Give the extent of all Plasmodium falciparum-infected red blood cells.
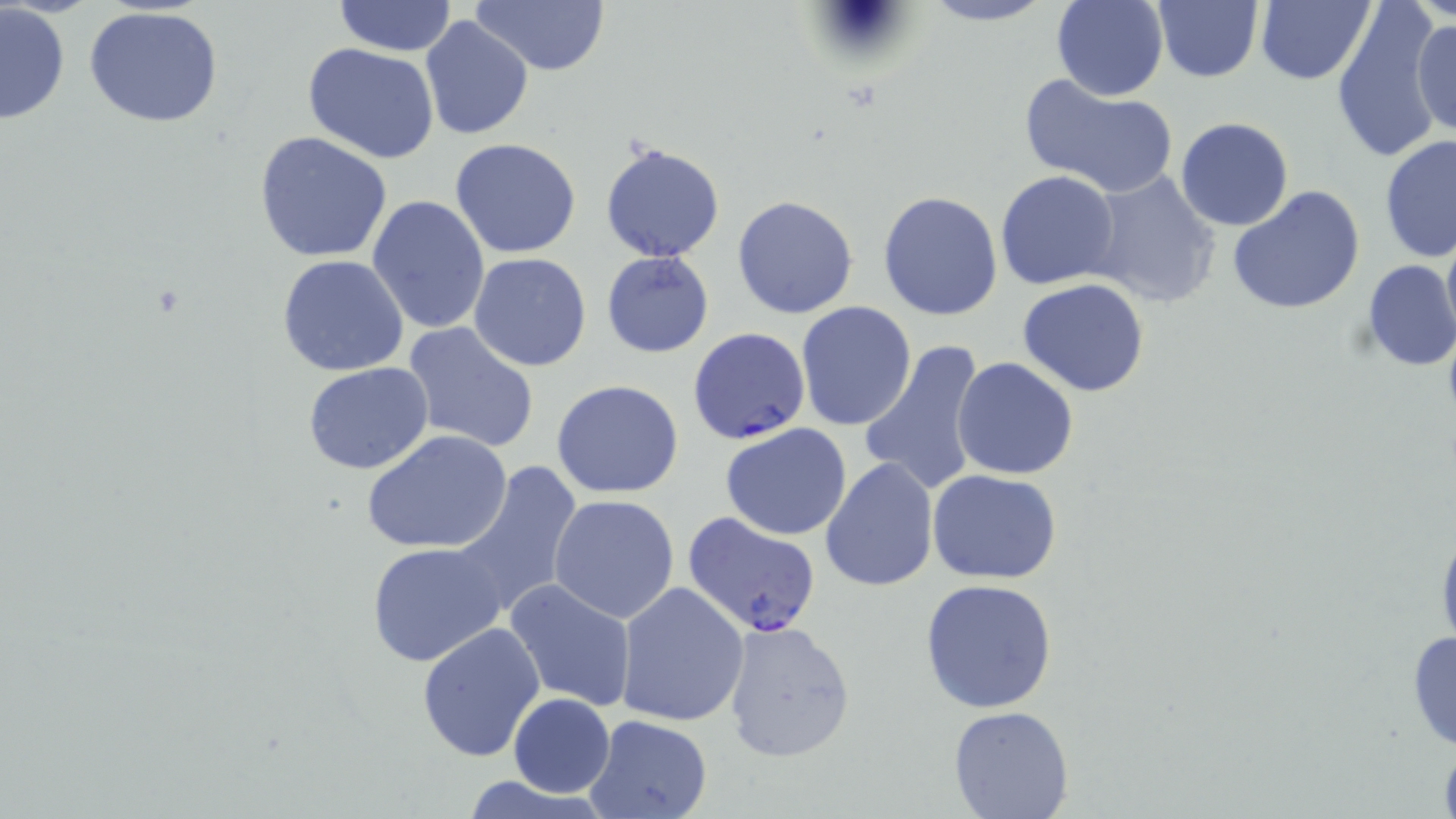

Approximate bounding boxes as (x1,y1)-(x2,y2) corner pairs in pixels.
Plasmodium falciparum-infected red blood cells: (688,326)-(811,445), (682,512)-(821,637).

slide-level diagnosis = Plasmodium falciparum
stain = May-Grünwald-Giemsa
modality = light microscopy
field of view = one of a larger specimen
uninfected red blood cell locations = approximate bounding boxes as (x1,y1)-(x2,y2) corner pairs in pixels: (468,0)-(610,77), (915,0)-(1058,27), (1050,0)-(1169,102), (1256,0)-(1377,87), (1151,1)-(1263,82), (332,2)-(456,55), (1,3)-(71,127), (1332,5)-(1442,164), (82,7)-(227,130), (1412,13)-(1455,143), (420,15)-(534,141), (301,43)-(442,166), (1018,73)-(1179,198), (1174,117)-(1294,232), (253,130)-(394,264), (1379,135)-(1456,266), (450,138)-(583,258), (599,139)-(727,264), (1085,170)-(1223,308), (994,171)-(1122,291), (1227,185)-(1367,316), (877,190)-(1004,322), (731,194)-(859,320), (368,195)-(491,337), (1440,220)-(1456,350), (601,250)-(714,359), (468,253)-(593,372), (277,254)-(409,376), (1359,260)-(1456,372), (1017,278)-(1150,398), (795,301)-(919,432), (402,322)-(541,455), (860,337)-(989,498), (951,357)-(1079,480), (302,362)-(435,475), (552,380)-(684,499), (719,423)-(853,541), (361,429)-(515,555), (819,456)-(939,593), (449,459)-(586,620), (928,469)-(1061,584), (549,494)-(680,624), (1434,516)-(1456,660), (366,541)-(510,669), (919,578)-(1060,713), (506,579)-(637,713), (616,582)-(750,726), (721,619)-(855,763), (417,622)-(547,762), (1405,626)-(1456,753), (508,694)-(614,798), (947,703)-(1076,819), (583,715)-(713,819)
image size = 1456×819 pixels
preparation = thin blood film
magnification = 1000x